Assess this cell for malaria.
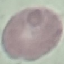
Uninfected.

capture: smartphone camera at the microscope eyepiece
preparation: thin blood smear
stain: Giemsa
image_type: automatically extracted cell patch, resized to 64 × 64 pixels